Point out each Plasmodium parasite and each leukocyte.
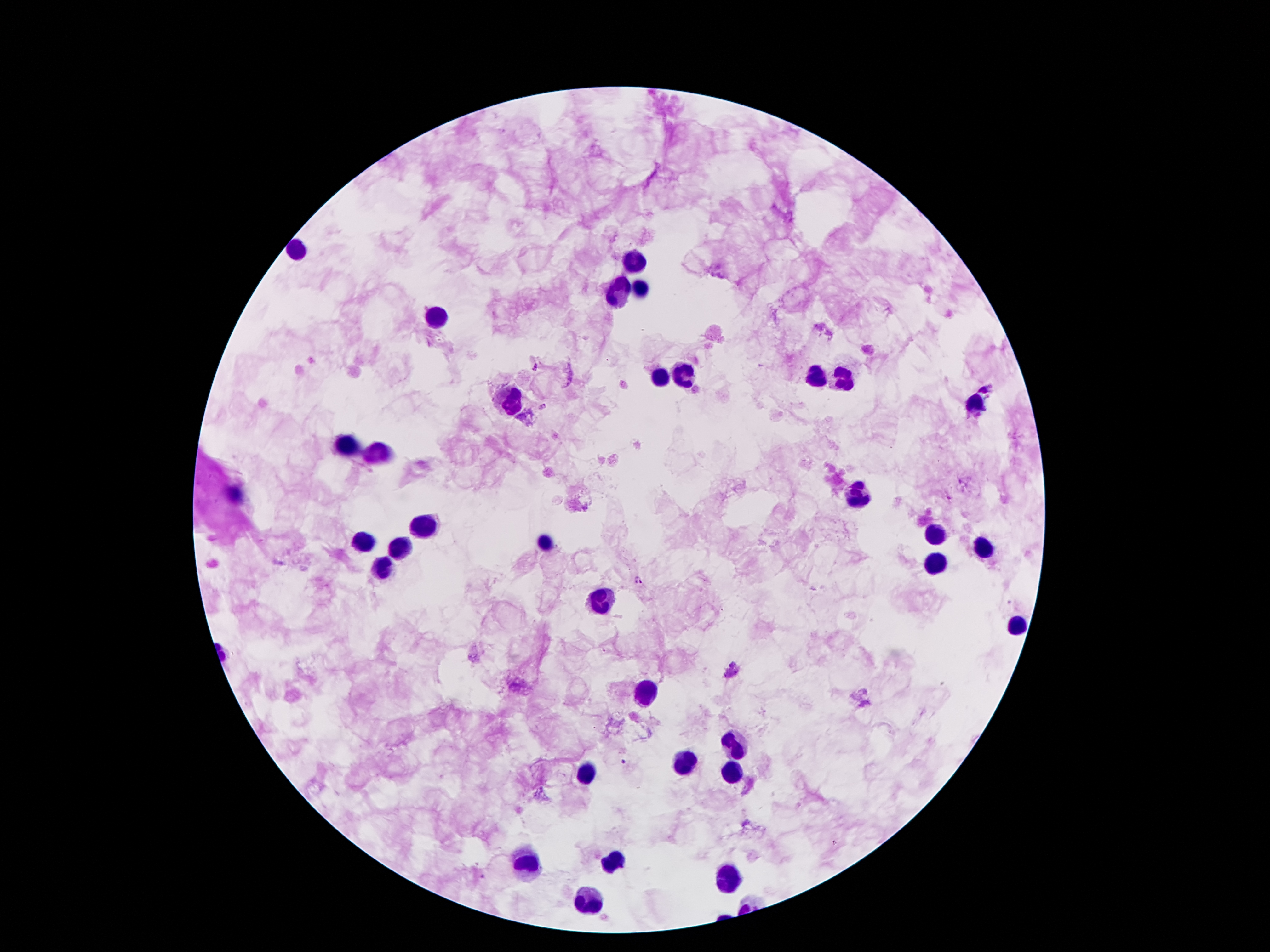

Approximate object centers, in pixels from the top-left corner.
Plasmodium parasites: (x=535, y=368), (x=543, y=407), (x=638, y=579), (x=731, y=671), (x=622, y=762).
Leukocytes: (x=297, y=250), (x=634, y=266), (x=622, y=288), (x=638, y=288), (x=438, y=314), (x=661, y=373), (x=818, y=375), (x=686, y=379), (x=840, y=380), (x=509, y=400), (x=974, y=404), (x=347, y=448), (x=379, y=454), (x=232, y=495), (x=856, y=495), (x=425, y=527), (x=933, y=534), (x=365, y=543), (x=545, y=543), (x=400, y=547), (x=983, y=547), (x=933, y=563), (x=384, y=566), (x=602, y=598), (x=1017, y=625), (x=647, y=693), (x=734, y=743), (x=686, y=763), (x=733, y=772), (x=584, y=775), (x=617, y=859), (x=527, y=864), (x=729, y=881), (x=592, y=902).

Summary:
  - Patient malaria status: positive for Plasmodium falciparum
  - Image size: 1270×952 pixels
  - Stain: Giemsa
  - Preparation: thick blood film
  - Capture: smartphone camera through the microscope eyepiece
  - Field of view: single
  - Magnification: 100x